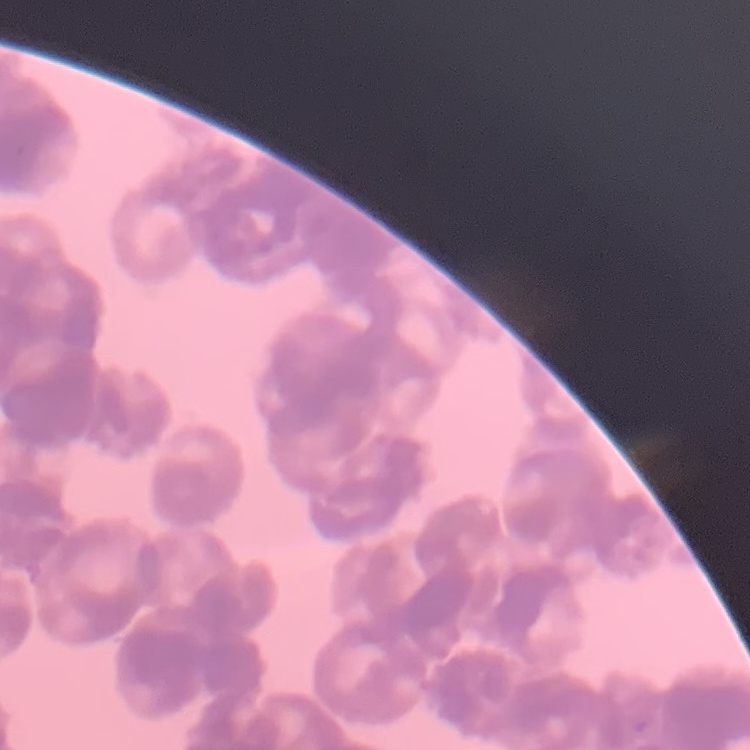
Summary:
  - Red blood cell morphology: rouleaux formation
  - Image type: one tile cut from a larger photomicrograph
  - Preparation: thin blood film
  - Stain: Field's or Giemsa